Report the malaria status of this cell.
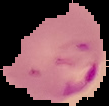

It is parasitized.

The area outside the segmented cell region is set to black. Image is 109×106 pixels. From a thin blood film.